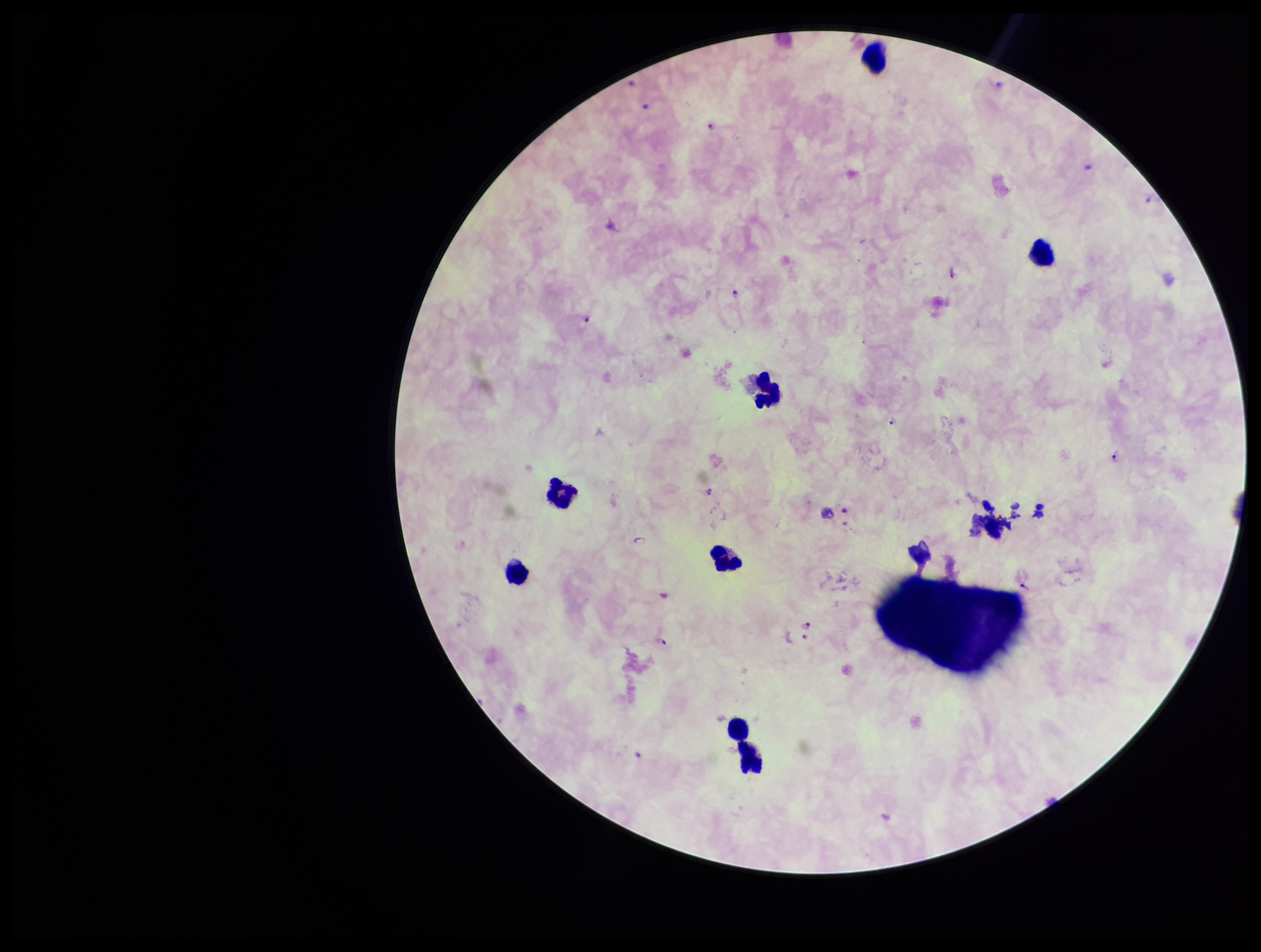

stain = Giemsa
preparation = thick blood smear
patient malaria status = positive
species reported for this patient = Plasmodium falciparum
capture = smartphone photograph through the microscope eyepiece
leukocyte count = 8
parasite count = 15
field of view = single
Plasmodium parasites = identified
image size = 1261×952 pixels